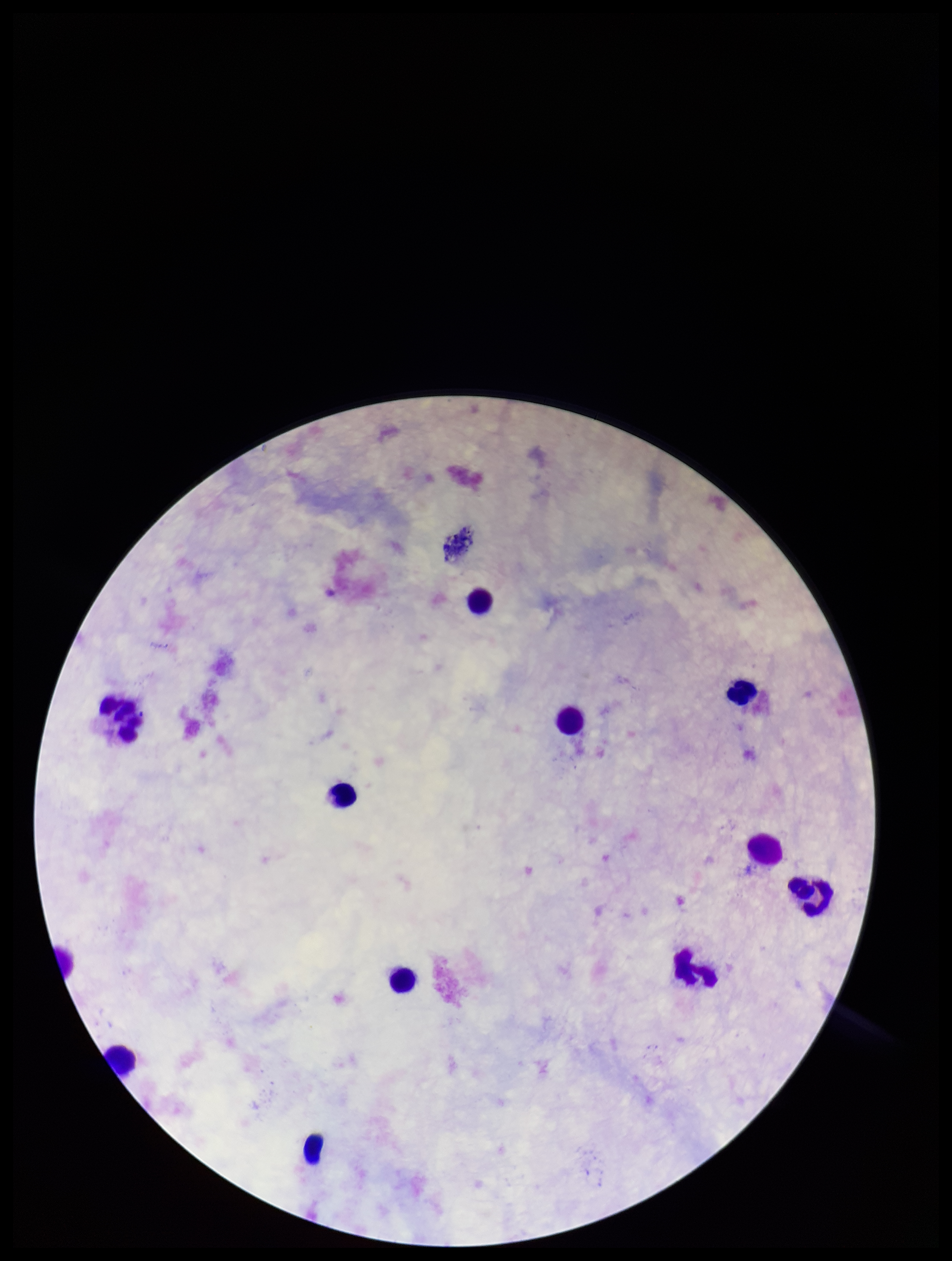
patient malaria status = negative
Plasmodium parasites = none seen
field of view = one from this slide
stain = Giemsa
capture = smartphone photograph through the microscope eyepiece
parasite count = 0
preparation = thick
image size = 952×1261 pixels
leukocyte count = 12